Outline platelets.
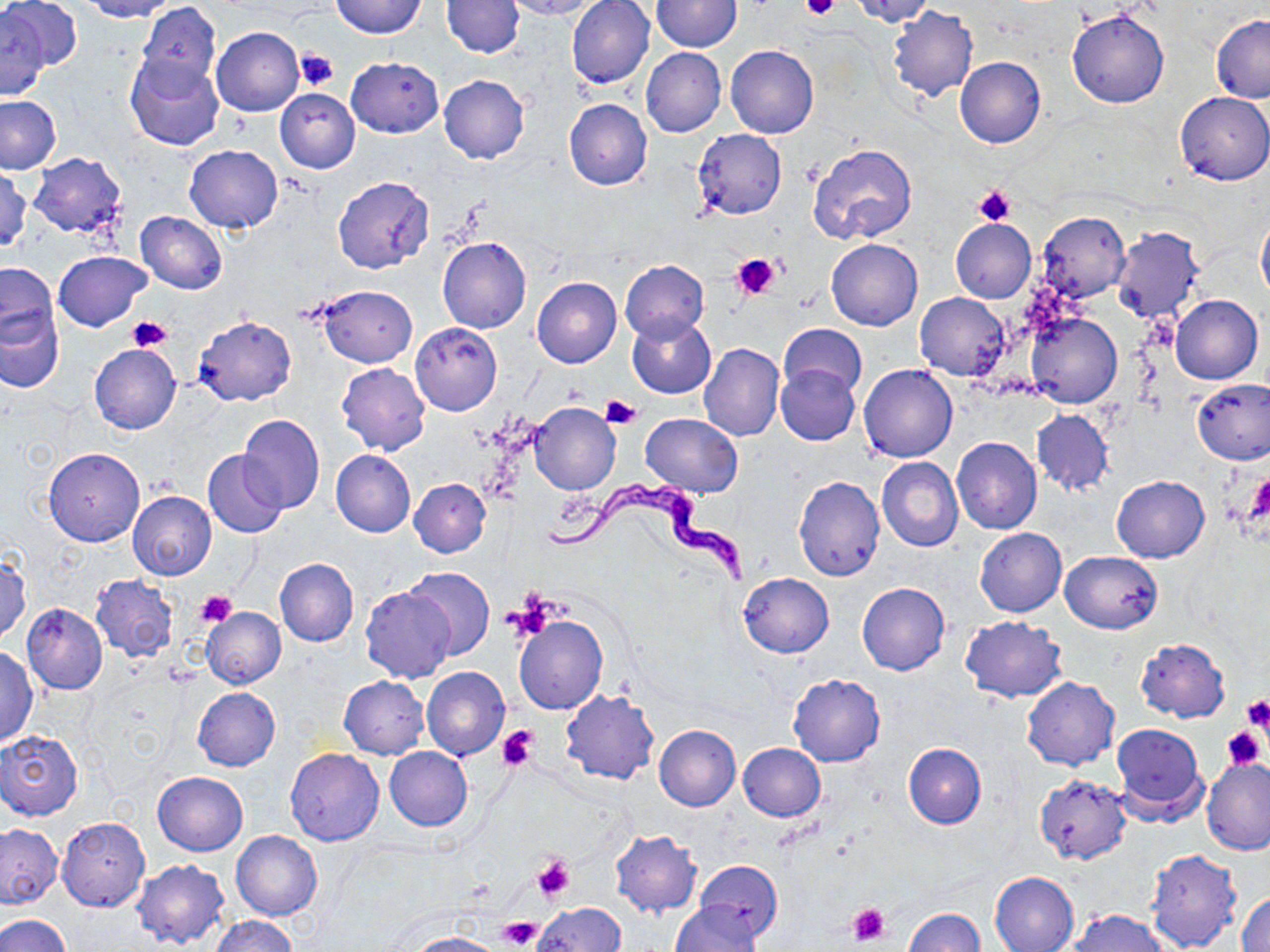
Approximate bounding boxes as [x1, y1, x2, y2] in pixels.
Platelets: [802, 0, 840, 22], [294, 48, 338, 91], [973, 185, 1016, 224], [733, 255, 781, 300], [127, 318, 173, 352], [600, 394, 640, 429], [1244, 471, 1270, 532], [196, 589, 237, 627], [509, 591, 560, 636], [1241, 694, 1269, 733], [1220, 724, 1265, 770], [497, 725, 539, 771], [533, 857, 574, 902], [846, 904, 891, 946], [497, 916, 543, 951].

Uninfected red blood cell locations: [2, 0, 81, 74], [80, 0, 175, 21], [331, 0, 427, 38], [501, 0, 598, 20], [566, 0, 655, 89], [848, 0, 934, 25], [442, 1, 523, 57], [650, 1, 741, 52], [135, 2, 218, 89], [887, 6, 978, 102], [1, 8, 49, 102], [1066, 10, 1170, 109], [1211, 15, 1270, 103], [212, 27, 303, 117], [725, 45, 820, 138], [642, 48, 727, 137], [125, 54, 225, 151], [346, 57, 443, 137], [954, 57, 1045, 149], [438, 75, 530, 163], [275, 88, 361, 173], [1176, 92, 1270, 186], [0, 95, 63, 175], [564, 99, 652, 191], [692, 128, 787, 220], [807, 143, 919, 247], [184, 144, 283, 232], [27, 153, 127, 237], [0, 167, 31, 252], [332, 175, 434, 273], [135, 211, 227, 293], [1036, 211, 1131, 304], [1257, 211, 1270, 302], [950, 217, 1036, 303], [1110, 227, 1204, 325], [437, 236, 531, 333], [826, 239, 923, 332], [55, 250, 151, 331], [620, 260, 708, 341], [1, 261, 60, 350], [531, 276, 621, 368], [315, 285, 418, 368], [916, 293, 1010, 380], [1170, 295, 1262, 384], [0, 306, 63, 392], [1027, 310, 1122, 408], [194, 315, 297, 406], [626, 315, 716, 398], [411, 322, 501, 415], [779, 324, 866, 400], [88, 343, 181, 434], [699, 343, 784, 441], [336, 363, 431, 455], [858, 364, 958, 464], [775, 365, 860, 445], [1191, 377, 1270, 465], [529, 402, 621, 495], [1030, 410, 1114, 495], [641, 412, 744, 497], [237, 413, 325, 513], [951, 437, 1042, 534], [43, 448, 145, 546], [203, 450, 288, 539], [331, 450, 416, 537], [877, 457, 963, 552], [1111, 475, 1210, 563], [793, 476, 884, 581], [409, 478, 490, 557], [128, 491, 216, 581], [975, 527, 1066, 617], [1059, 551, 1162, 633], [0, 553, 31, 643], [275, 557, 358, 646], [402, 566, 494, 660], [739, 572, 834, 657], [90, 574, 178, 662], [857, 582, 949, 675], [361, 586, 456, 683], [22, 604, 108, 693], [201, 606, 285, 688], [514, 615, 607, 715], [960, 615, 1066, 702], [1135, 638, 1230, 723], [1, 646, 38, 747], [422, 665, 510, 761], [788, 673, 885, 767], [338, 676, 429, 759], [1022, 676, 1120, 771], [192, 687, 281, 771], [561, 689, 659, 785], [1110, 722, 1208, 821], [653, 724, 740, 810], [1219, 727, 1267, 771], [0, 728, 84, 821], [738, 742, 826, 821], [902, 743, 986, 829], [384, 747, 472, 830], [285, 748, 384, 845], [1203, 757, 1270, 855], [153, 771, 248, 856], [1034, 774, 1132, 865], [56, 815, 150, 912], [1, 823, 64, 909], [610, 829, 702, 917], [232, 830, 323, 921], [1146, 848, 1241, 952], [133, 857, 231, 949], [695, 860, 783, 942], [989, 871, 1079, 952], [1237, 890, 1270, 952], [670, 901, 764, 952], [533, 903, 626, 951], [906, 908, 985, 952], [1068, 909, 1169, 952], [0, 915, 70, 952], [211, 915, 296, 952], [404, 932, 505, 952]. Trypanosoma brucei locations: [537, 477, 752, 586]. Slide-level diagnosis: Trypanosoma brucei. Light microscopy. Image is 1270×952 pixels. Thin blood film. May-Grünwald-Giemsa stain. Single field of view. 1000x magnification.